Classify this cell by malaria status.
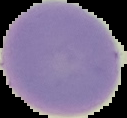

It is uninfected.

{
  "image_type": "segmented cell region with the area outside set to black",
  "preparation": "thin blood smear",
  "image_size": "127×118 pixels"
}